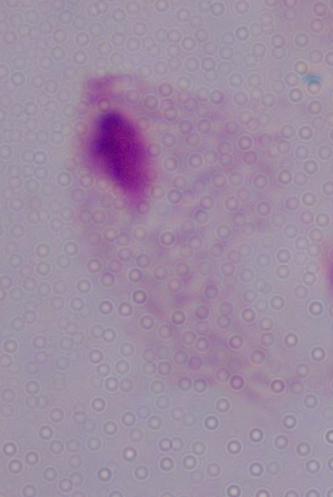

{
  "identification": "trichomonad",
  "magnification": "1000x",
  "modality": "micrograph"
}